Assess this cell for malaria.
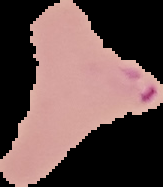

Parasitized.

From a thin blood film. Image is 163×187 pixels. Cell region segmented out of the field of view; the surrounding area is masked to black.